Report the malaria status of this cell.
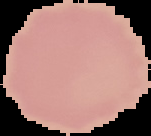
Uninfected.

preparation: thin blood film
image_type: segmented cell region with the area outside set to black
image_size: 151×136 pixels